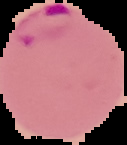
Summary:
  - Image type: segmented cell region with the area outside set to black
  - Image size: 127×145 pixels
  - Malaria status: parasitized
  - Preparation: thin blood smear